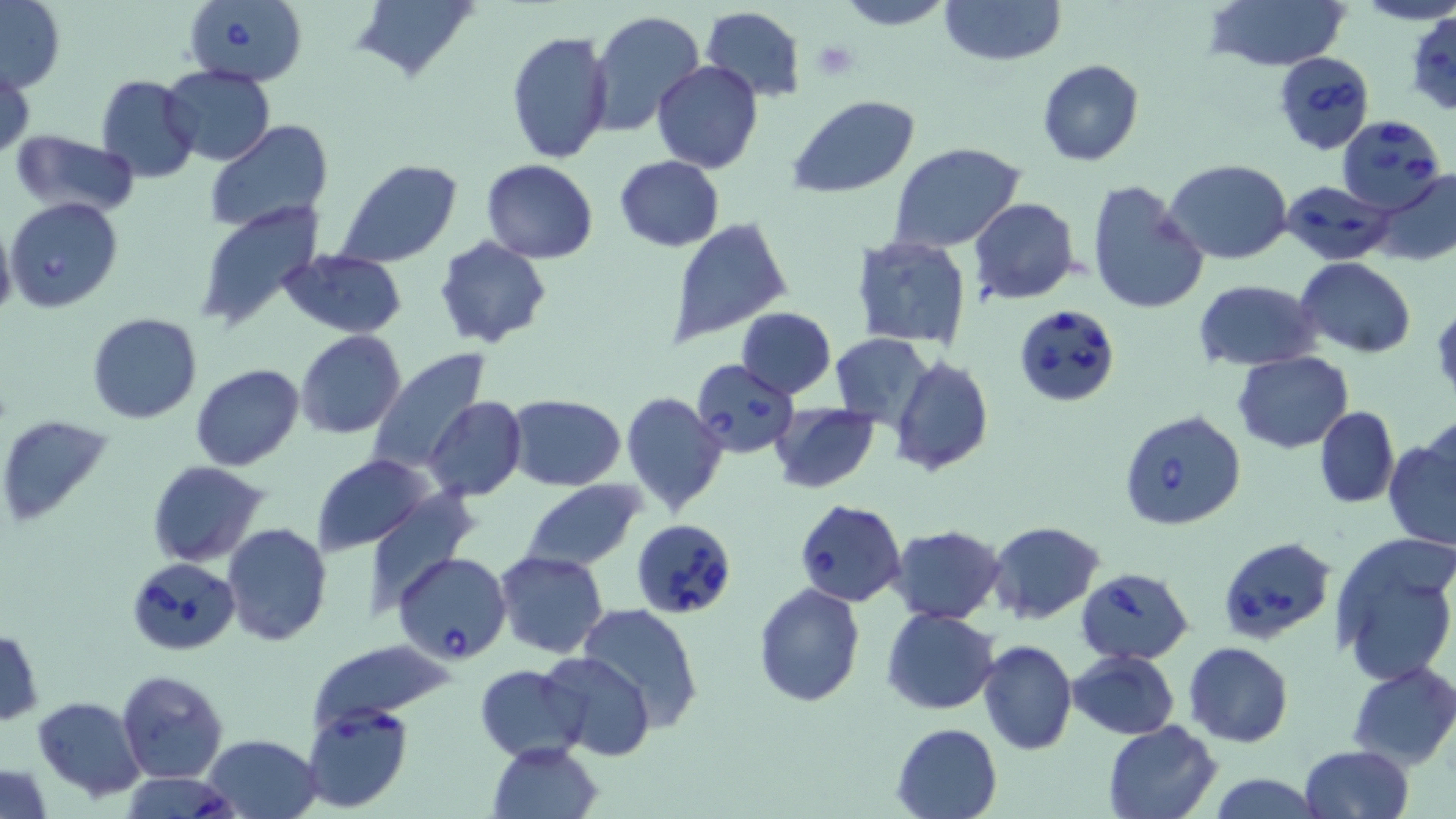
Summary:
  - Coordinate format: approximate bounding boxes as named x1/y1/x2/y2 corners in pixels
  - Babesia divergens-infected red blood cell locations: (x1=181, y1=0, x2=307, y2=87), (x1=1273, y1=52, x2=1375, y2=152), (x1=1336, y1=115, x2=1445, y2=213), (x1=1279, y1=179, x2=1395, y2=266), (x1=5, y1=196, x2=124, y2=313), (x1=1013, y1=303, x2=1119, y2=406), (x1=692, y1=359, x2=800, y2=457), (x1=1120, y1=411, x2=1245, y2=531), (x1=794, y1=500, x2=907, y2=607), (x1=632, y1=519, x2=738, y2=621), (x1=1216, y1=535, x2=1337, y2=645), (x1=394, y1=551, x2=512, y2=664), (x1=127, y1=556, x2=241, y2=659), (x1=1076, y1=566, x2=1193, y2=664), (x1=301, y1=700, x2=414, y2=811), (x1=120, y1=772, x2=237, y2=819)
  - Uninfected red blood cell locations: (x1=833, y1=0, x2=956, y2=29), (x1=939, y1=0, x2=1066, y2=66), (x1=1204, y1=0, x2=1352, y2=73), (x1=0, y1=1, x2=64, y2=92), (x1=350, y1=1, x2=481, y2=84), (x1=701, y1=6, x2=806, y2=102), (x1=589, y1=10, x2=703, y2=136), (x1=1406, y1=11, x2=1456, y2=115), (x1=507, y1=28, x2=613, y2=165), (x1=1037, y1=59, x2=1144, y2=167), (x1=651, y1=61, x2=762, y2=173), (x1=160, y1=63, x2=276, y2=165), (x1=1, y1=67, x2=35, y2=159), (x1=97, y1=74, x2=200, y2=184), (x1=789, y1=96, x2=920, y2=199), (x1=204, y1=121, x2=333, y2=237), (x1=11, y1=131, x2=141, y2=217), (x1=887, y1=142, x2=1026, y2=252), (x1=613, y1=157, x2=725, y2=251), (x1=334, y1=159, x2=461, y2=269), (x1=481, y1=159, x2=599, y2=263), (x1=1164, y1=159, x2=1294, y2=265), (x1=1371, y1=168, x2=1456, y2=267), (x1=1086, y1=180, x2=1211, y2=316), (x1=969, y1=198, x2=1078, y2=303), (x1=194, y1=201, x2=327, y2=334), (x1=663, y1=216, x2=794, y2=347), (x1=0, y1=219, x2=16, y2=325), (x1=850, y1=235, x2=972, y2=349), (x1=433, y1=236, x2=554, y2=350), (x1=279, y1=249, x2=406, y2=338), (x1=1295, y1=256, x2=1416, y2=357), (x1=1192, y1=279, x2=1323, y2=371), (x1=735, y1=307, x2=836, y2=398), (x1=86, y1=313, x2=202, y2=424), (x1=295, y1=331, x2=407, y2=439), (x1=830, y1=332, x2=934, y2=430), (x1=366, y1=351, x2=492, y2=476), (x1=1232, y1=352, x2=1354, y2=453), (x1=889, y1=358, x2=994, y2=475), (x1=190, y1=363, x2=304, y2=470), (x1=620, y1=392, x2=731, y2=517), (x1=505, y1=394, x2=628, y2=490), (x1=425, y1=397, x2=526, y2=502), (x1=770, y1=402, x2=880, y2=492), (x1=1314, y1=405, x2=1399, y2=508), (x1=0, y1=415, x2=112, y2=527), (x1=1384, y1=436, x2=1456, y2=552), (x1=312, y1=454, x2=435, y2=555), (x1=146, y1=460, x2=271, y2=568), (x1=519, y1=480, x2=644, y2=571), (x1=356, y1=487, x2=480, y2=612), (x1=988, y1=521, x2=1104, y2=623), (x1=222, y1=522, x2=333, y2=647), (x1=887, y1=523, x2=1006, y2=624), (x1=1329, y1=532, x2=1456, y2=685), (x1=493, y1=549, x2=610, y2=660), (x1=753, y1=582, x2=865, y2=706), (x1=577, y1=603, x2=704, y2=728), (x1=881, y1=608, x2=999, y2=714), (x1=0, y1=628, x2=43, y2=725), (x1=978, y1=639, x2=1077, y2=754), (x1=315, y1=640, x2=457, y2=727), (x1=1185, y1=642, x2=1294, y2=747), (x1=1068, y1=649, x2=1179, y2=739), (x1=538, y1=651, x2=656, y2=760), (x1=1348, y1=661, x2=1456, y2=769), (x1=475, y1=665, x2=588, y2=761), (x1=116, y1=669, x2=229, y2=783), (x1=33, y1=696, x2=148, y2=801), (x1=1100, y1=720, x2=1222, y2=819), (x1=891, y1=722, x2=1002, y2=819), (x1=200, y1=734, x2=325, y2=818), (x1=486, y1=741, x2=603, y2=819), (x1=1299, y1=744, x2=1415, y2=819), (x1=0, y1=763, x2=53, y2=817), (x1=1208, y1=774, x2=1324, y2=818)
  - Platelet locations: (x1=811, y1=40, x2=860, y2=82)
  - Slide-level diagnosis: Babesia divergens
  - Stain: May-Grünwald-Giemsa
  - Image size: 1456×819 pixels
  - Preparation: thin blood smear
  - Magnification: 1000x
  - Modality: optical microscopy
  - Field of view: one of a larger specimen